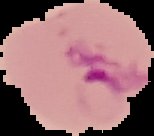

Summary:
  - Result: Plasmodium parasites detected
  - Image type: segmented cell region on a black background
  - Preparation: thin blood film
  - Image size: 154×136 pixels